Assess this cell for malaria.
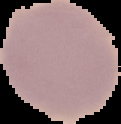

Uninfected.

preparation = thin blood film
image type = cell region segmented out of the field of view; surrounding area masked to black
image size = 121×124 pixels